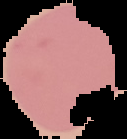
Summary:
  - Image size: 127×139 pixels
  - Malaria status: uninfected
  - Image type: segmented cell region on a black background
  - Preparation: thin blood film